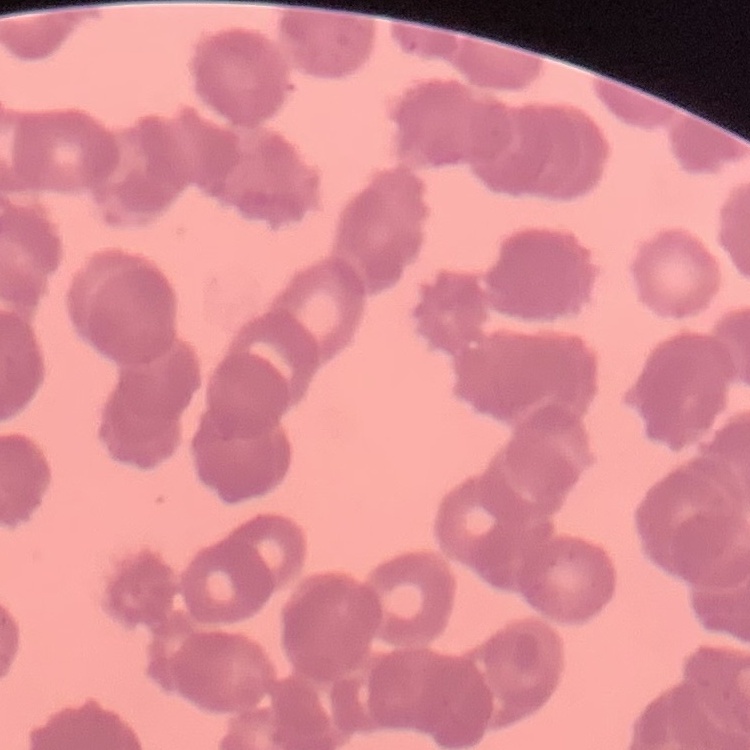

red_blood_cell_morphology: rouleaux formation
preparation: thin blood smear
image_type: one tile cut from a larger photomicrograph
stain: Field's or Giemsa